Describe the morphology of the erythrocytes.
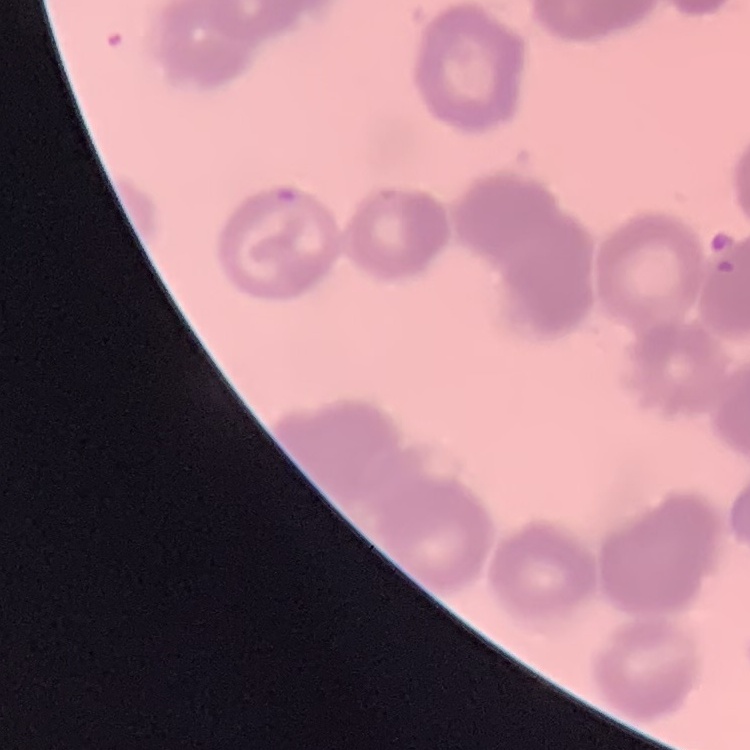

They show rouleaux formation.

Thin peripheral smear. Field's or Giemsa stain. One tile cut from a larger photomicrograph.